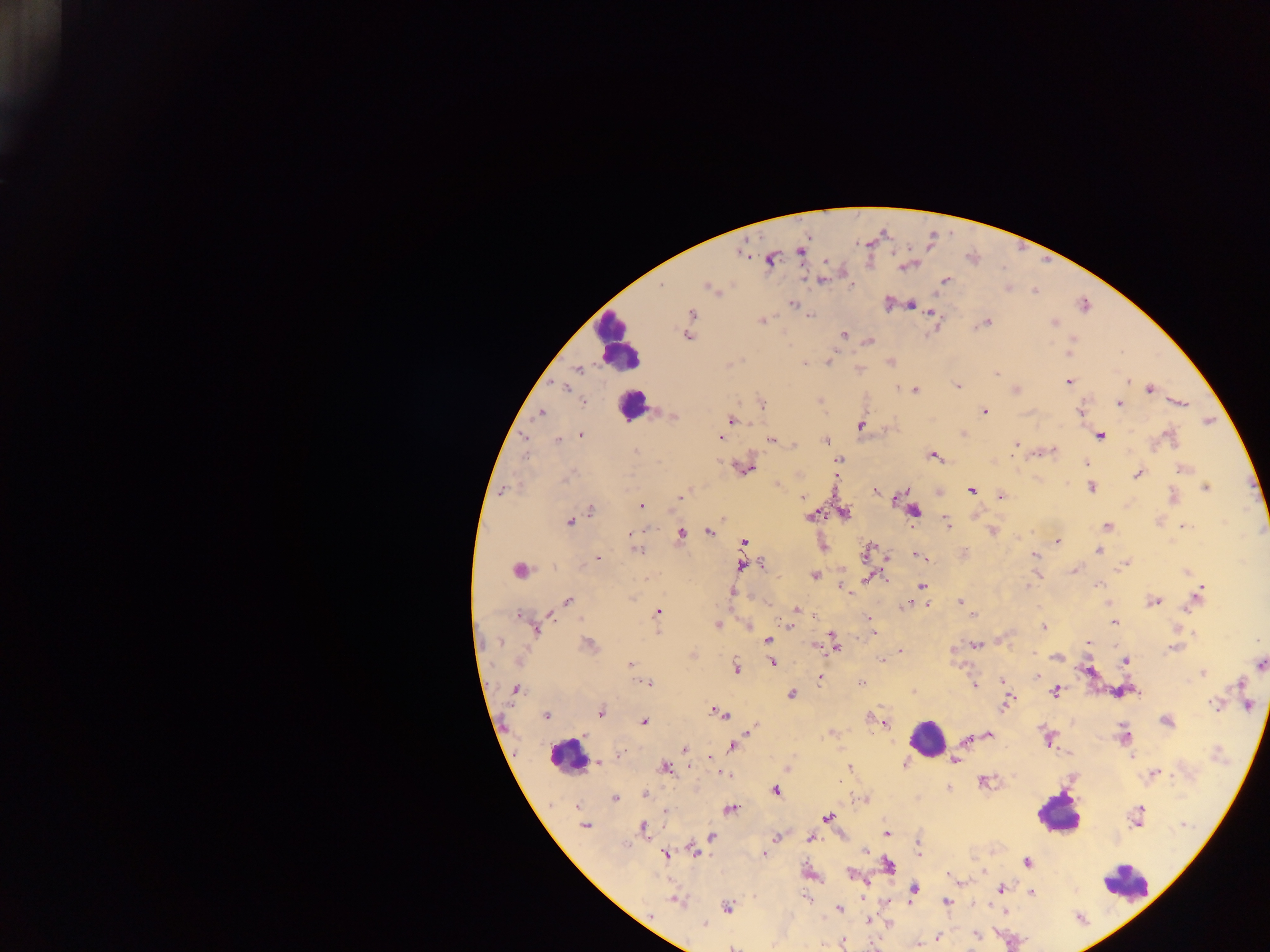
Approximate centers as (x, y) in pixels.
Summary:
  - Leukocyte locations: (617, 342), (632, 405), (519, 570), (926, 739), (566, 757), (1058, 814), (1126, 881)
  - Malaria parasite locations: (801, 252), (771, 259), (825, 261), (945, 280), (821, 281), (661, 285), (708, 287), (1035, 291), (792, 304), (911, 304), (1084, 305), (692, 314), (932, 314), (810, 316), (762, 320), (986, 323), (1053, 323), (844, 334), (687, 336), (869, 341), (1069, 354), (829, 362), (804, 364), (578, 369), (996, 373), (1069, 381), (1130, 381), (958, 386), (566, 389), (1016, 390), (1150, 390), (915, 391), (584, 402), (1120, 403), (1181, 403), (762, 404), (985, 411), (541, 413), (1080, 413), (670, 415), (731, 420), (860, 425), (581, 435), (1100, 435), (1169, 436), (524, 437), (720, 437), (771, 440), (558, 441), (825, 441), (1017, 444), (795, 445), (1053, 450), (635, 451), (932, 456), (839, 460), (1087, 463), (746, 469), (1182, 469), (1138, 474), (568, 477), (777, 485), (1091, 488), (1205, 488), (971, 490), (876, 491), (1001, 496), (1172, 496), (680, 497), (899, 497), (803, 498), (641, 506), (590, 510), (914, 511), (844, 513), (812, 516), (569, 522), (946, 522), (1107, 526), (1185, 526), (709, 531), (630, 532), (681, 534), (1057, 541), (744, 543), (637, 550), (1098, 551), (867, 552), (917, 555), (1034, 555), (599, 558), (1126, 563), (762, 565), (742, 566), (1074, 571), (1186, 571), (814, 575), (868, 578), (921, 585), (1098, 585), (1027, 586), (841, 587), (733, 593), (1197, 595), (568, 601), (1154, 601), (1108, 602), (960, 603), (904, 604), (925, 604), (795, 610), (657, 613), (972, 615), (550, 616), (518, 617), (581, 618), (868, 618), (1114, 623), (787, 624), (717, 625), (749, 625), (1043, 627), (537, 630), (833, 637), (768, 640), (1088, 642), (500, 643), (976, 644), (589, 645), (815, 645), (836, 645), (954, 649), (1173, 649), (901, 651), (1035, 654), (1056, 657), (882, 660), (1125, 661), (772, 662), (630, 664), (1260, 664), (737, 668), (1202, 673), (1036, 675), (819, 679), (1002, 681), (648, 683), (861, 683), (1240, 683), (975, 685), (515, 689), (1055, 691), (791, 694), (1006, 704), (1214, 704), (1247, 704), (601, 713), (721, 714), (545, 715), (869, 718), (1166, 721), (644, 722), (885, 724), (753, 730), (989, 735), (1124, 737), (967, 740), (733, 746), (685, 748), (623, 752), (711, 757), (959, 757), (955, 761), (598, 762), (904, 764), (850, 768), (664, 769), (1156, 774), (725, 775), (983, 781), (948, 788), (775, 791), (644, 794), (615, 798), (577, 807), (730, 810), (1139, 811), (665, 812), (827, 818), (585, 826), (643, 829), (887, 833), (711, 836), (776, 837), (810, 838), (918, 844), (694, 850), (865, 850), (919, 854), (665, 855), (764, 855), (1027, 863), (888, 865), (851, 874), (1000, 889), (914, 890), (1031, 893), (805, 898), (677, 901), (946, 902), (728, 907), (839, 908), (868, 921), (704, 925), (976, 935), (938, 937), (843, 942), (919, 946), (732, 947)
  - Country: Ghana
  - Capture: mobile-phone photograph through a microscope
  - Image size: 1270×952 pixels
  - Field of view: single
  - Preparation: thick blood film